Locate and identify every blood parasite.
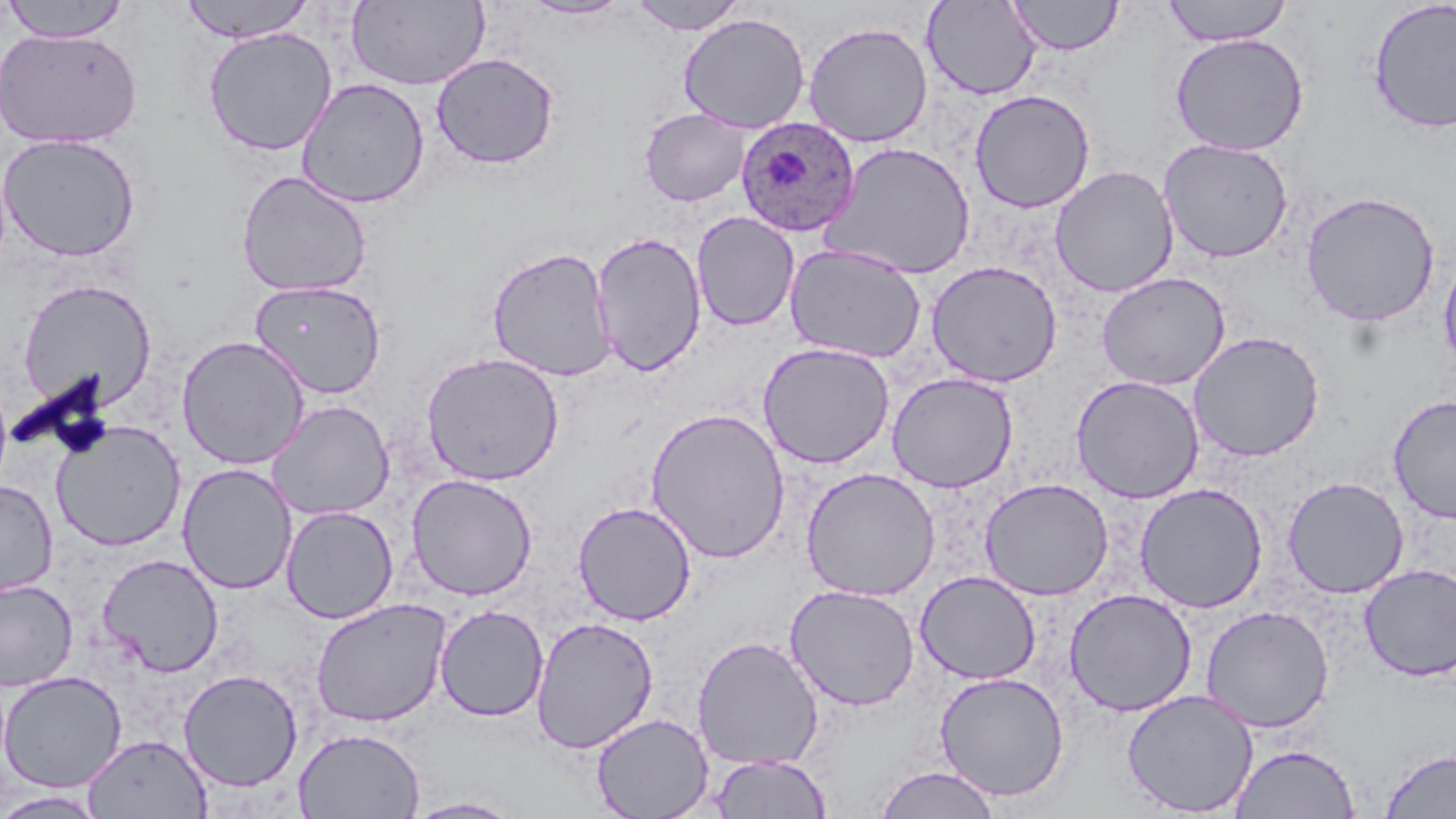

Approximate bounding boxes as (x1, y1, x2, y2) in pixels.
Plasmodium ovale-infected red blood cells: (736, 116, 860, 238).
No Plasmodium falciparum, Plasmodium malariae, Plasmodium vivax, Babesia divergens, or Trypanosoma brucei observed.

Uninfected red blood cell locations: (181, 0, 314, 43), (346, 0, 491, 90), (520, 0, 633, 20), (628, 0, 748, 35), (922, 0, 1042, 101), (1008, 0, 1123, 56), (1162, 0, 1293, 46), (2, 1, 133, 41), (1367, 1, 1456, 134), (678, 13, 811, 134), (803, 22, 933, 147), (202, 26, 338, 156), (1, 27, 143, 149), (1170, 33, 1309, 156), (431, 52, 560, 170), (296, 77, 430, 209), (969, 89, 1095, 213), (639, 108, 751, 207), (0, 132, 141, 262), (1158, 138, 1294, 263), (823, 142, 976, 280), (1049, 165, 1179, 298), (236, 170, 373, 298), (1300, 191, 1440, 327), (690, 211, 800, 331), (590, 231, 707, 377), (784, 243, 926, 364), (487, 246, 617, 382), (1438, 247, 1456, 374), (926, 260, 1063, 388), (1096, 271, 1231, 391), (17, 278, 158, 412), (249, 279, 388, 398), (1187, 331, 1325, 462), (176, 335, 310, 470), (757, 342, 895, 469), (421, 352, 565, 486), (886, 372, 1019, 493), (1071, 375, 1204, 504), (1387, 395, 1456, 524), (267, 400, 394, 520), (645, 407, 791, 563), (51, 419, 186, 551), (177, 463, 298, 595), (800, 467, 940, 601), (406, 474, 538, 601), (979, 477, 1114, 600), (1282, 477, 1409, 598), (0, 480, 58, 597), (1134, 482, 1269, 613), (572, 500, 697, 626), (281, 505, 399, 624), (97, 553, 224, 677), (1359, 563, 1456, 681), (915, 570, 1041, 685), (0, 578, 78, 691), (785, 584, 920, 711), (1063, 588, 1197, 717), (310, 597, 452, 727), (434, 604, 549, 722), (1200, 604, 1335, 733), (530, 616, 659, 754), (691, 635, 824, 770), (178, 669, 303, 792), (0, 670, 127, 793), (934, 671, 1070, 801), (1121, 689, 1259, 817), (590, 712, 714, 819), (293, 727, 425, 819), (83, 734, 212, 818), (1231, 743, 1360, 819), (1380, 748, 1456, 818), (708, 753, 831, 818), (874, 765, 1002, 819), (0, 790, 108, 818), (403, 797, 527, 818). Slide-level diagnosis: Plasmodium ovale. Single field of view. Optical microscopy. Image is 1456×819 pixels. May-Grünwald-Giemsa-stained preparation. Thin blood film. 1000x magnification.